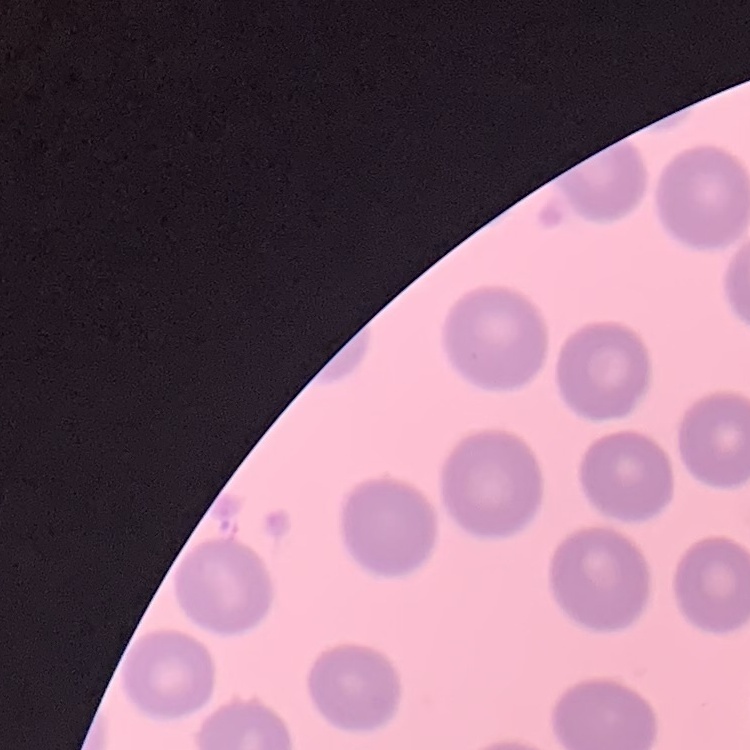

Summary:
  - Red blood cell morphology: no rouleaux formation
  - Image type: square crop of a larger photomicrograph
  - Stain: Field's or Giemsa
  - Preparation: thin blood film